State which parasite is depicted.
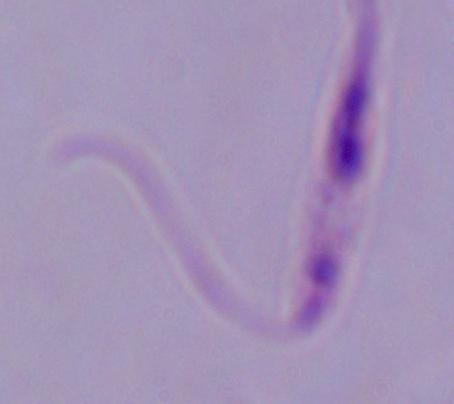

Leishmania.

Captured at 1000x magnification. Photomicrograph.